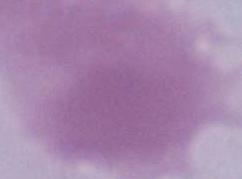
Summary:
  - Identification: red blood cell
  - Magnification: 1000x
  - Modality: photomicrograph